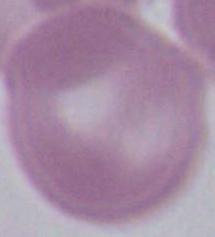
identification = red blood cell
magnification = 1000x
modality = micrograph